Assess this cell for malaria.
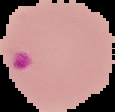

It is parasitized.

From a thin blood smear. Segmented cell region on a black background. Image is 115×112 pixels.